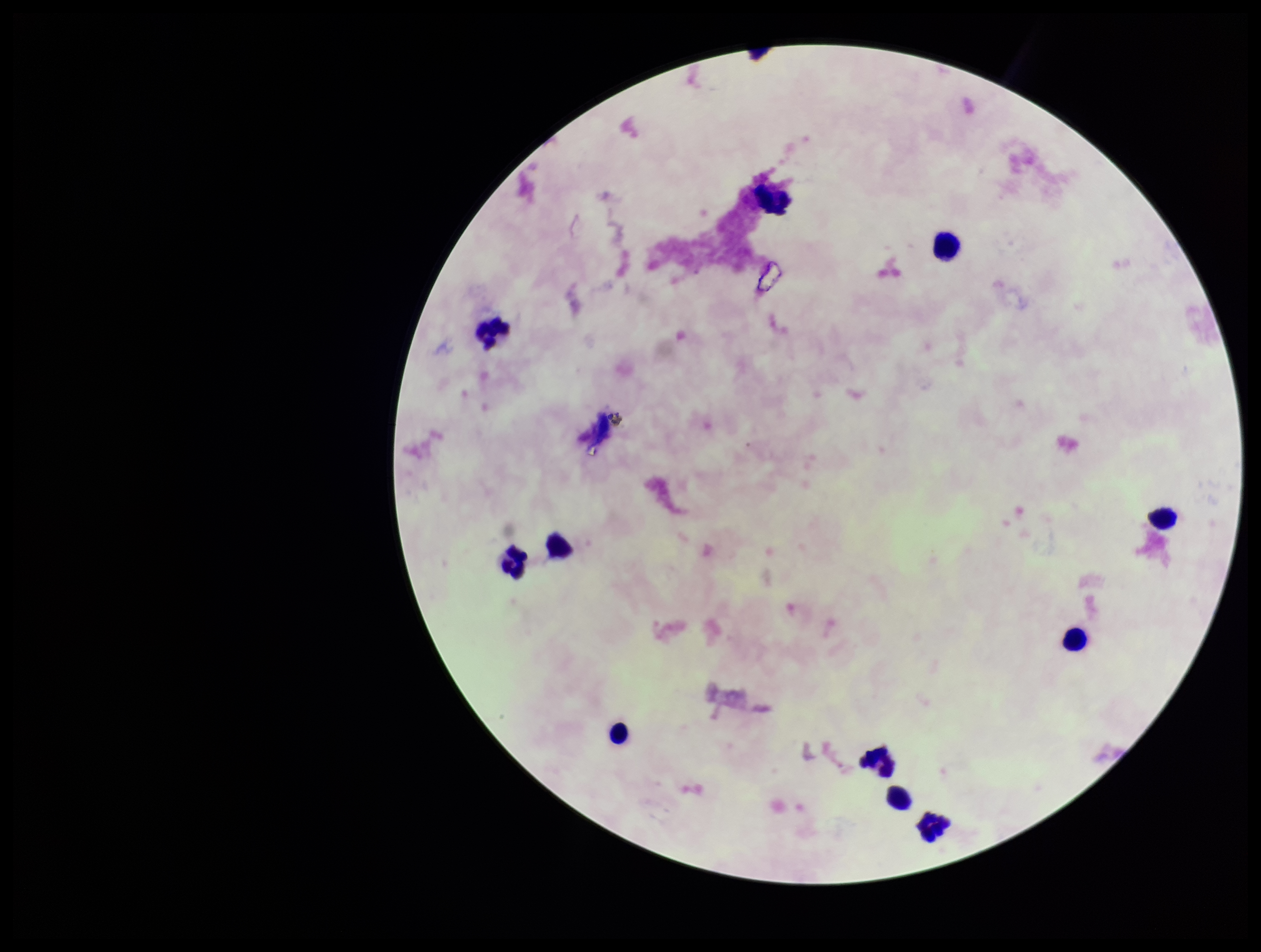
field_of_view: single
capture: smartphone photograph through the microscope eyepiece
image_size: 1261×952 pixels
parasite_count: 0
stain: Giemsa
leukocyte_count: 11
patient_malaria_status: negative
plasmodium_parasites: none seen
preparation: thick blood smear